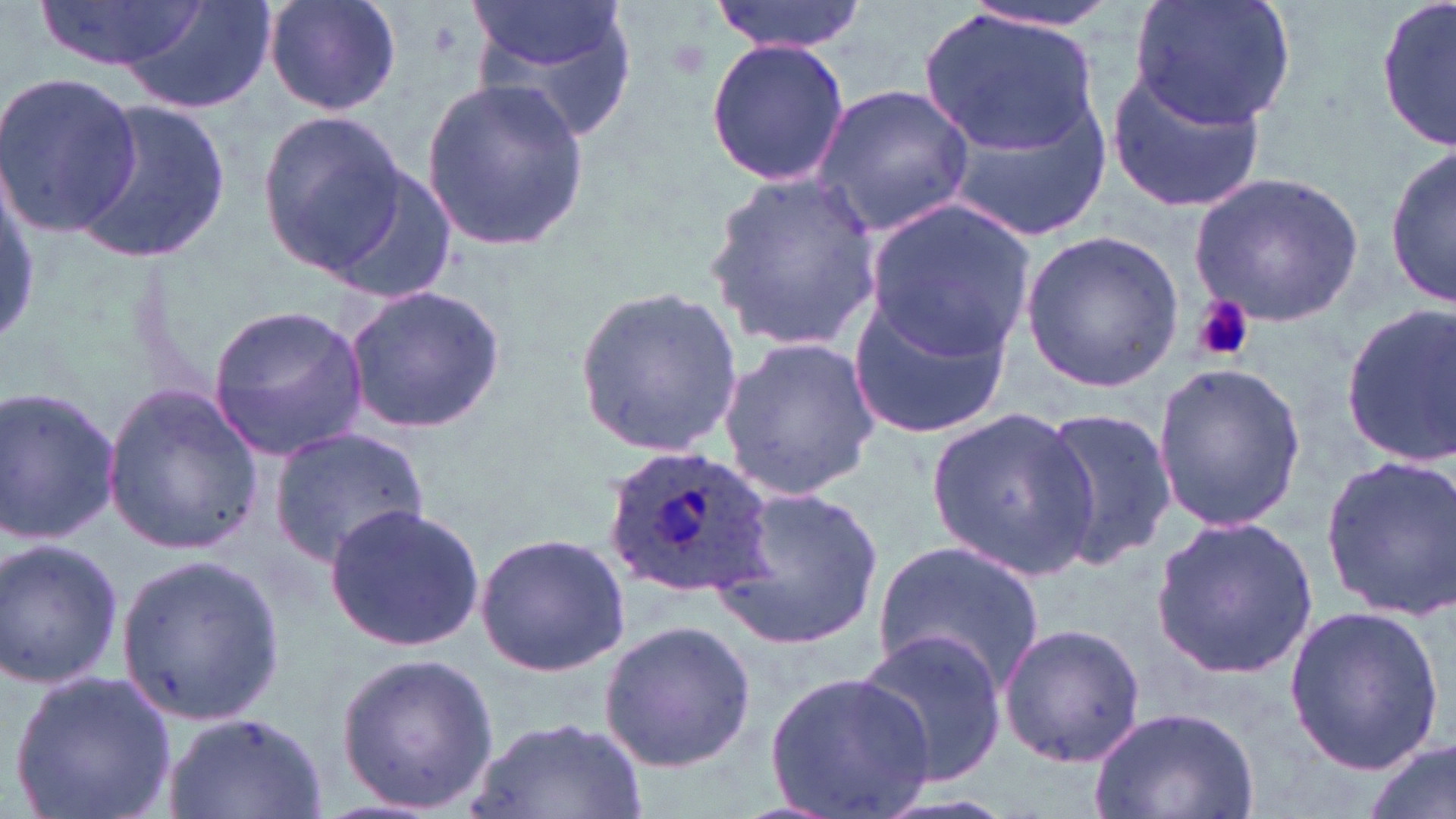
Approximate bounding boxes as named x1/y1/x2/y2 corners in pixels. Platelet locations: (x1=1192, y1=296, x2=1254, y2=363). Uninfected red blood cell locations: (x1=117, y1=0, x2=281, y2=114), (x1=261, y1=0, x2=404, y2=116), (x1=465, y1=0, x2=641, y2=147), (x1=708, y1=0, x2=872, y2=56), (x1=1130, y1=0, x2=1296, y2=130), (x1=1377, y1=0, x2=1455, y2=153), (x1=36, y1=1, x2=203, y2=74), (x1=959, y1=1, x2=1121, y2=37), (x1=920, y1=8, x2=1101, y2=153), (x1=704, y1=39, x2=851, y2=187), (x1=1106, y1=63, x2=1271, y2=213), (x1=0, y1=72, x2=140, y2=235), (x1=418, y1=74, x2=589, y2=252), (x1=810, y1=84, x2=974, y2=235), (x1=938, y1=93, x2=1111, y2=243), (x1=71, y1=100, x2=233, y2=263), (x1=259, y1=109, x2=409, y2=270), (x1=1387, y1=145, x2=1455, y2=311), (x1=319, y1=164, x2=461, y2=306), (x1=1187, y1=171, x2=1366, y2=325), (x1=703, y1=172, x2=884, y2=349), (x1=864, y1=199, x2=1035, y2=360), (x1=1021, y1=229, x2=1184, y2=389), (x1=341, y1=285, x2=509, y2=435), (x1=575, y1=285, x2=744, y2=458), (x1=845, y1=290, x2=1015, y2=438), (x1=208, y1=301, x2=370, y2=462), (x1=1339, y1=305, x2=1456, y2=464), (x1=715, y1=334, x2=881, y2=503), (x1=1151, y1=362, x2=1307, y2=534), (x1=102, y1=385, x2=266, y2=554), (x1=0, y1=387, x2=121, y2=548), (x1=922, y1=404, x2=1100, y2=578), (x1=1038, y1=405, x2=1174, y2=572), (x1=269, y1=428, x2=431, y2=565), (x1=1318, y1=455, x2=1456, y2=622), (x1=710, y1=484, x2=883, y2=655), (x1=324, y1=504, x2=486, y2=652), (x1=1149, y1=513, x2=1320, y2=682), (x1=475, y1=531, x2=630, y2=677), (x1=870, y1=534, x2=1046, y2=698), (x1=0, y1=537, x2=124, y2=691), (x1=115, y1=552, x2=283, y2=724), (x1=1283, y1=605, x2=1444, y2=775), (x1=599, y1=616, x2=758, y2=773), (x1=998, y1=621, x2=1147, y2=769), (x1=856, y1=631, x2=1009, y2=788), (x1=334, y1=651, x2=498, y2=813), (x1=9, y1=670, x2=175, y2=818), (x1=766, y1=670, x2=935, y2=818), (x1=1089, y1=702, x2=1259, y2=819), (x1=163, y1=712, x2=331, y2=819), (x1=465, y1=714, x2=647, y2=819), (x1=1360, y1=735, x2=1456, y2=819). Plasmodium ovale-infected red blood cell locations: (x1=600, y1=449, x2=779, y2=604). Slide-level diagnosis: Plasmodium ovale. One field of a larger specimen. Optical microscopy. Captured at 1000x magnification. Image is 1456×819 pixels. May-Grünwald-Giemsa stain. Thin blood film.